Give the position of every leukocyte visible.
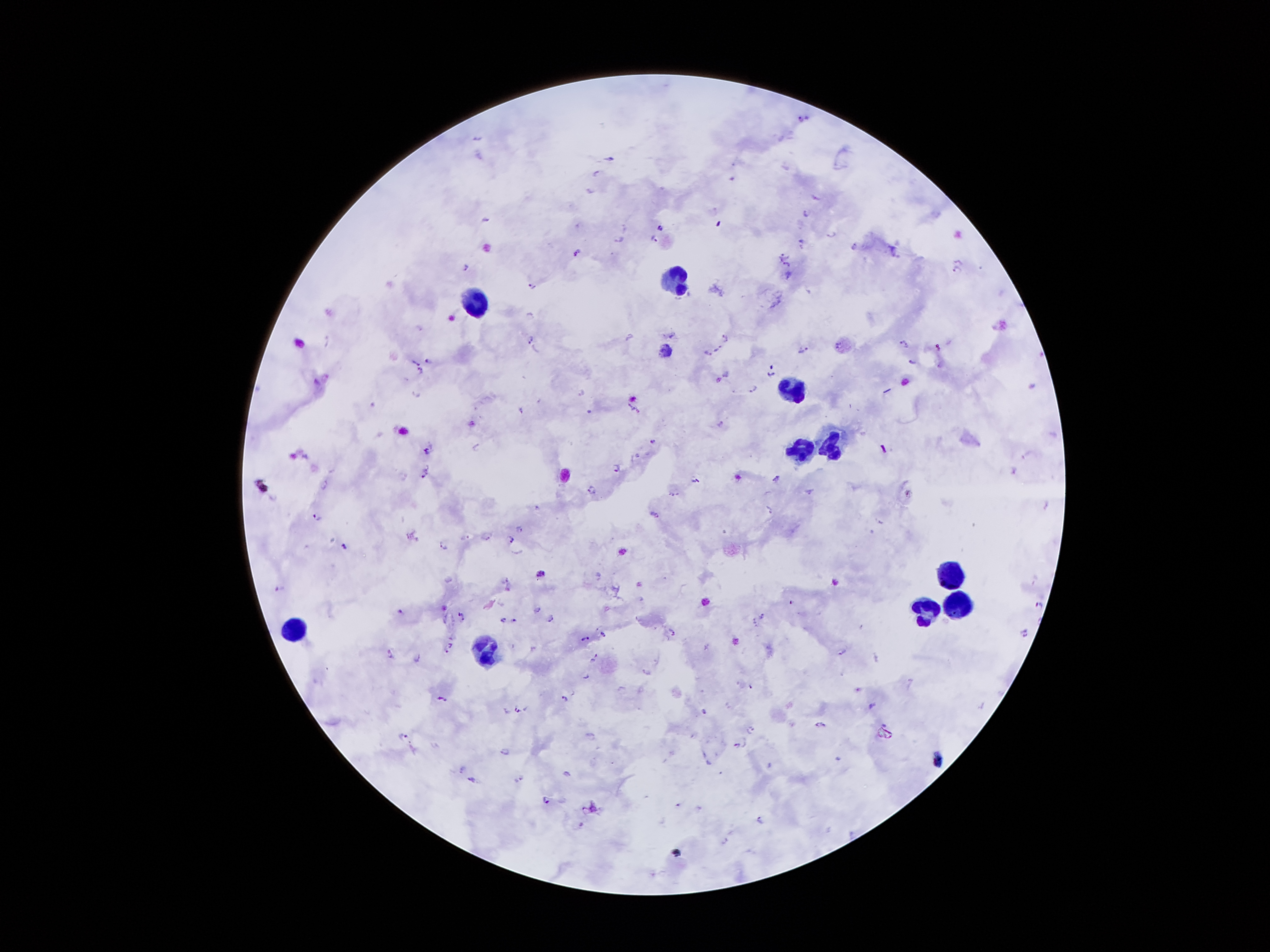
Approximate object centers, in pixels from the top-left corner.
Leukocytes: (x=682, y=278), (x=472, y=297), (x=789, y=389), (x=826, y=445), (x=801, y=448), (x=949, y=574), (x=958, y=605), (x=925, y=613), (x=295, y=631), (x=483, y=649).

Malaria parasite locations: (x=800, y=117), (x=476, y=137), (x=611, y=157), (x=595, y=171), (x=590, y=189), (x=815, y=197), (x=805, y=212), (x=624, y=226), (x=659, y=227), (x=830, y=234), (x=653, y=238), (x=618, y=239), (x=801, y=243), (x=853, y=247), (x=575, y=252), (x=785, y=255), (x=786, y=265), (x=465, y=267), (x=958, y=268), (x=788, y=275), (x=532, y=286), (x=670, y=334), (x=725, y=335), (x=530, y=339), (x=325, y=342), (x=902, y=343), (x=937, y=346), (x=803, y=348), (x=717, y=349), (x=707, y=354), (x=427, y=360), (x=912, y=362), (x=416, y=363), (x=770, y=370), (x=420, y=371), (x=1033, y=386), (x=751, y=388), (x=416, y=392), (x=581, y=393), (x=522, y=407), (x=633, y=408), (x=720, y=423), (x=653, y=441), (x=477, y=446), (x=882, y=449), (x=424, y=451), (x=638, y=454), (x=1027, y=455), (x=616, y=468), (x=1013, y=468), (x=422, y=472), (x=776, y=478), (x=697, y=480), (x=324, y=483), (x=591, y=490), (x=810, y=492), (x=673, y=494), (x=909, y=494), (x=1045, y=504), (x=536, y=505), (x=769, y=509), (x=657, y=515), (x=316, y=516), (x=881, y=522), (x=520, y=529), (x=487, y=536), (x=465, y=537), (x=511, y=538), (x=443, y=545), (x=344, y=546), (x=1034, y=577), (x=279, y=587), (x=791, y=602), (x=1039, y=603), (x=535, y=607), (x=400, y=609), (x=762, y=614), (x=461, y=615), (x=502, y=618), (x=514, y=619), (x=549, y=619), (x=753, y=622), (x=861, y=625), (x=602, y=631), (x=1024, y=631), (x=672, y=632), (x=585, y=639), (x=449, y=646), (x=840, y=651), (x=875, y=656), (x=593, y=657), (x=418, y=660), (x=645, y=673), (x=586, y=675), (x=738, y=684), (x=750, y=686), (x=619, y=690), (x=441, y=698), (x=562, y=698), (x=871, y=706), (x=505, y=709), (x=518, y=710), (x=704, y=712), (x=820, y=724), (x=750, y=728), (x=406, y=737), (x=738, y=746), (x=505, y=751), (x=461, y=767), (x=472, y=778), (x=520, y=779), (x=546, y=800), (x=677, y=804), (x=760, y=818), (x=577, y=823), (x=724, y=840). Giemsa stain. Patient malaria status: positive for Plasmodium falciparum. Thick blood film. Smartphone photograph taken through the microscope eyepiece. 100x magnification. Single field of view. Image is 1270×952 pixels.